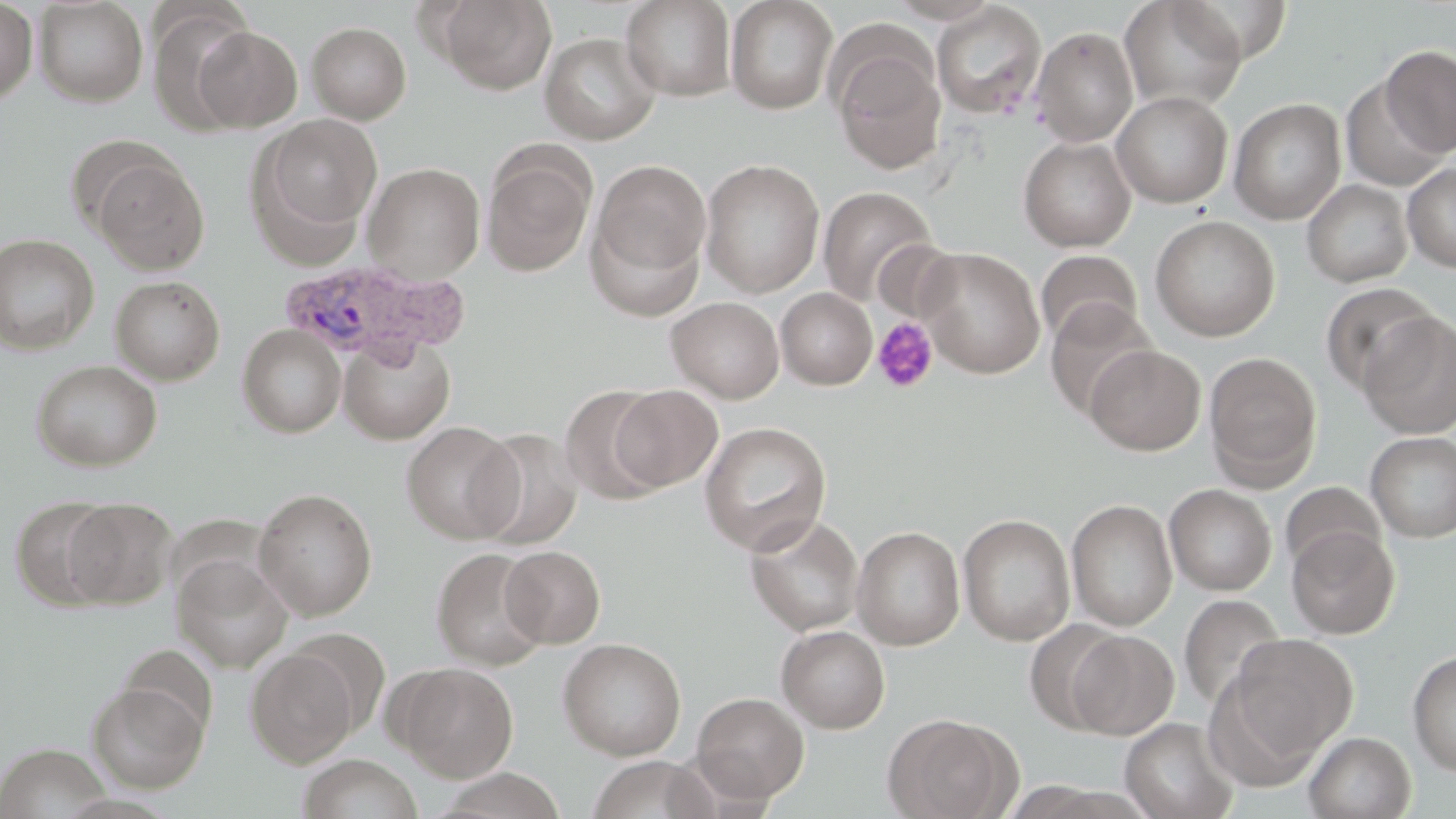

slide-level diagnosis = Plasmodium vivax
field of view = single
preparation = thin blood film
modality = light microscopy
stain = May-Grünwald-Giemsa
image size = 1456×819 pixels
platelet locations = approximate bounding boxes as [x1, y1, x2, y2] in pixels: [872, 317, 939, 393]
uninfected red blood cell locations = approximate bounding boxes as [x1, y1, x2, y2] in pixels: [34, 0, 149, 107], [436, 0, 557, 95], [620, 0, 737, 101], [725, 0, 838, 115], [1119, 0, 1247, 113], [0, 1, 38, 106], [930, 2, 1047, 120], [147, 5, 260, 135], [306, 21, 412, 124], [190, 25, 303, 132], [1031, 26, 1139, 147], [539, 32, 661, 145], [831, 44, 946, 175], [1382, 45, 1456, 157], [1339, 75, 1450, 192], [1111, 91, 1233, 208], [1229, 98, 1346, 225], [257, 114, 383, 239], [64, 133, 180, 238], [1018, 136, 1136, 252], [481, 145, 596, 278], [92, 155, 209, 274], [592, 159, 710, 280], [700, 159, 825, 298], [363, 163, 485, 283], [1402, 163, 1456, 272], [1302, 179, 1413, 287], [817, 186, 939, 309], [585, 210, 707, 322], [1149, 215, 1280, 342], [0, 234, 99, 354], [871, 239, 963, 325], [915, 247, 1046, 379], [1035, 250, 1142, 348], [111, 276, 225, 384], [1319, 281, 1439, 395], [776, 287, 877, 389], [666, 297, 784, 403], [1044, 299, 1159, 420], [1358, 312, 1456, 439], [237, 324, 347, 438], [339, 335, 455, 444], [1085, 344, 1206, 455], [1205, 351, 1322, 486], [31, 360, 163, 471], [560, 385, 669, 505], [609, 385, 723, 491], [401, 421, 523, 544], [699, 422, 832, 555], [471, 429, 584, 551], [1365, 432, 1456, 542], [1280, 482, 1387, 577], [1164, 484, 1276, 596], [253, 488, 378, 621], [10, 495, 121, 611], [61, 497, 178, 609], [1065, 499, 1178, 631], [957, 513, 1075, 645], [744, 514, 864, 636], [851, 525, 965, 650], [1286, 526, 1399, 639], [500, 545, 605, 648], [431, 548, 549, 670], [172, 555, 293, 674], [1178, 594, 1286, 714], [1024, 619, 1128, 734], [776, 625, 891, 733], [288, 628, 392, 736], [1068, 630, 1180, 739], [1226, 633, 1359, 761], [558, 638, 686, 760], [119, 645, 218, 739], [245, 648, 359, 767], [1407, 650, 1456, 778], [395, 663, 519, 782], [87, 681, 208, 793], [691, 692, 809, 803], [882, 713, 1019, 818], [1119, 717, 1239, 819], [1304, 731, 1416, 819], [0, 743, 112, 817], [297, 754, 422, 819], [585, 755, 719, 819], [433, 768, 567, 819]
magnification = 1000x
Plasmodium vivax-infected red blood cell locations = approximate bounding boxes as [x1, y1, x2, y2] in pixels: [276, 258, 472, 367]